State which parasite is depicted.
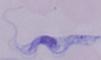

A trypanosome.

1000x magnification. Micrograph.